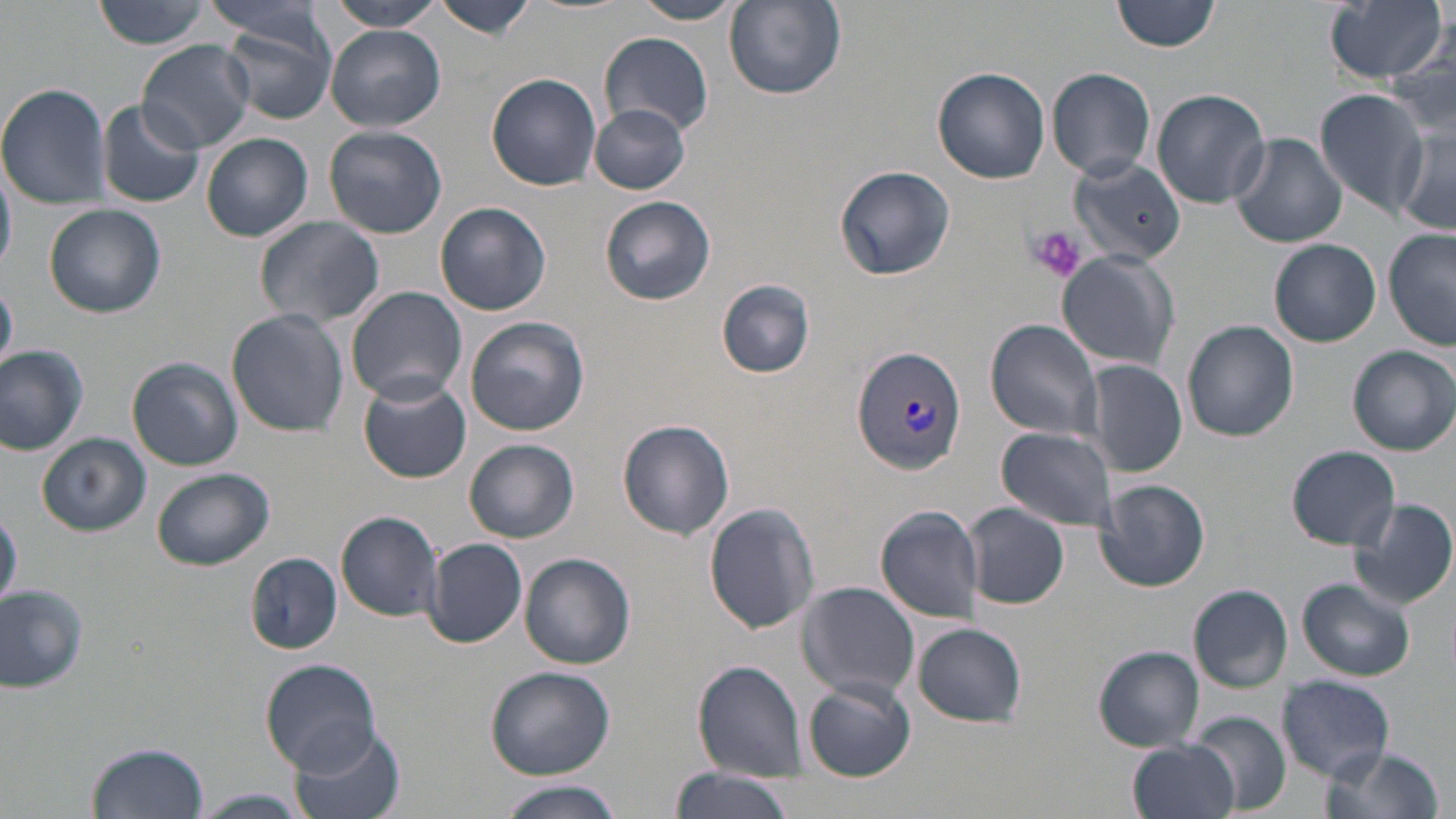
Summary:
  - Coordinate format: approximate bounding boxes as named x1/y1/x2/y2 corners in pixels
  - Plasmodium vivax-infected red blood cell locations: (x1=850, y1=344, x2=970, y2=477)
  - Uninfected red blood cell locations: (x1=89, y1=0, x2=217, y2=50), (x1=321, y1=0, x2=448, y2=31), (x1=434, y1=0, x2=537, y2=40), (x1=627, y1=0, x2=746, y2=24), (x1=1113, y1=0, x2=1223, y2=54), (x1=1324, y1=0, x2=1448, y2=83), (x1=724, y1=1, x2=847, y2=101), (x1=201, y1=2, x2=331, y2=45), (x1=213, y1=11, x2=338, y2=123), (x1=326, y1=25, x2=446, y2=132), (x1=598, y1=31, x2=716, y2=138), (x1=137, y1=39, x2=256, y2=154), (x1=931, y1=67, x2=1050, y2=185), (x1=1045, y1=67, x2=1157, y2=180), (x1=487, y1=73, x2=602, y2=190), (x1=0, y1=82, x2=112, y2=210), (x1=1150, y1=87, x2=1271, y2=208), (x1=1316, y1=89, x2=1428, y2=213), (x1=97, y1=100, x2=205, y2=209), (x1=589, y1=103, x2=691, y2=194), (x1=324, y1=124, x2=448, y2=239), (x1=1394, y1=125, x2=1455, y2=233), (x1=201, y1=133, x2=314, y2=242), (x1=1229, y1=134, x2=1348, y2=249), (x1=0, y1=156, x2=17, y2=276), (x1=1069, y1=157, x2=1186, y2=267), (x1=836, y1=165, x2=954, y2=281), (x1=600, y1=195, x2=715, y2=305), (x1=435, y1=201, x2=552, y2=316), (x1=43, y1=202, x2=166, y2=318), (x1=254, y1=215, x2=386, y2=329), (x1=1382, y1=230, x2=1455, y2=350), (x1=1268, y1=238, x2=1382, y2=347), (x1=1057, y1=251, x2=1180, y2=372), (x1=717, y1=279, x2=815, y2=378), (x1=0, y1=281, x2=17, y2=371), (x1=346, y1=286, x2=468, y2=403), (x1=228, y1=309, x2=348, y2=437), (x1=465, y1=317, x2=588, y2=436), (x1=985, y1=319, x2=1106, y2=442), (x1=1183, y1=321, x2=1298, y2=442), (x1=0, y1=343, x2=89, y2=454), (x1=1348, y1=345, x2=1456, y2=456), (x1=127, y1=357, x2=243, y2=471), (x1=1081, y1=360, x2=1188, y2=477), (x1=359, y1=379, x2=471, y2=483), (x1=617, y1=419, x2=735, y2=540), (x1=996, y1=426, x2=1119, y2=533), (x1=38, y1=434, x2=149, y2=536), (x1=465, y1=439, x2=579, y2=543), (x1=1286, y1=445, x2=1400, y2=551), (x1=151, y1=466, x2=274, y2=571), (x1=1096, y1=479, x2=1210, y2=592), (x1=1349, y1=498, x2=1456, y2=610), (x1=705, y1=501, x2=821, y2=634), (x1=963, y1=502, x2=1070, y2=609), (x1=0, y1=508, x2=21, y2=610), (x1=874, y1=508, x2=986, y2=623), (x1=336, y1=510, x2=445, y2=621), (x1=424, y1=537, x2=528, y2=646), (x1=519, y1=552, x2=637, y2=668), (x1=246, y1=554, x2=341, y2=655), (x1=1295, y1=578, x2=1416, y2=682), (x1=796, y1=582, x2=920, y2=702), (x1=0, y1=584, x2=88, y2=693), (x1=1188, y1=585, x2=1294, y2=693), (x1=913, y1=622, x2=1027, y2=726), (x1=1093, y1=647, x2=1205, y2=752), (x1=261, y1=659, x2=382, y2=773), (x1=693, y1=660, x2=808, y2=779), (x1=484, y1=665, x2=616, y2=779), (x1=1277, y1=673, x2=1396, y2=781), (x1=803, y1=679, x2=916, y2=782), (x1=1185, y1=709, x2=1291, y2=816), (x1=291, y1=724, x2=407, y2=819), (x1=1127, y1=738, x2=1240, y2=819), (x1=87, y1=741, x2=209, y2=818), (x1=1315, y1=746, x2=1444, y2=819), (x1=670, y1=768, x2=792, y2=819), (x1=494, y1=780, x2=627, y2=819), (x1=187, y1=789, x2=313, y2=819)
  - Platelet locations: (x1=1026, y1=226, x2=1086, y2=284)
  - Slide-level diagnosis: Plasmodium vivax
  - Magnification: 1000x
  - Modality: optical microscopy
  - Field of view: one of a larger specimen
  - Stain: May-Grünwald-Giemsa
  - Image size: 1456×819 pixels
  - Preparation: thin blood smear